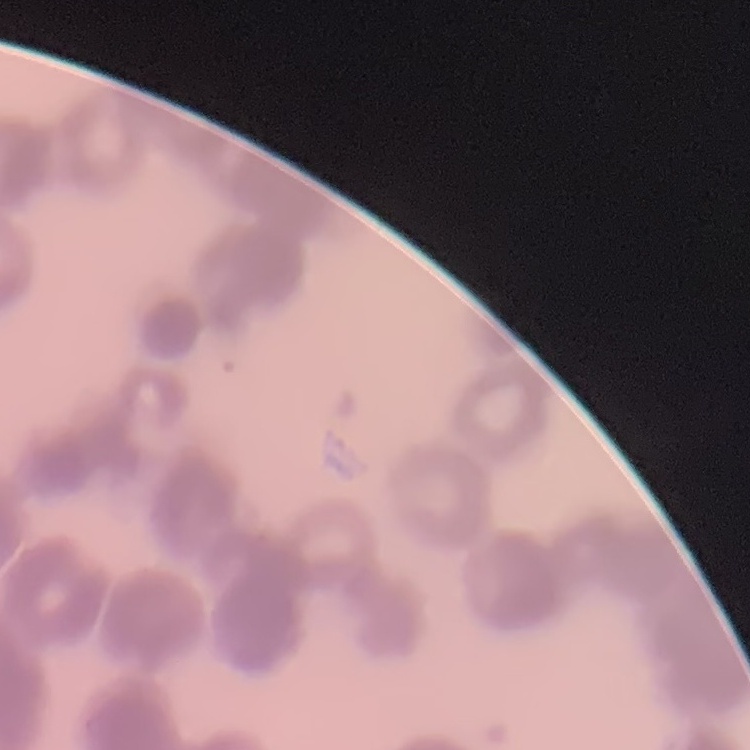

{
  "erythrocyte_morphology": "rouleaux formation",
  "stain": "Field's or Giemsa",
  "image_type": "square crop of a larger photomicrograph",
  "preparation": "thin blood film"
}